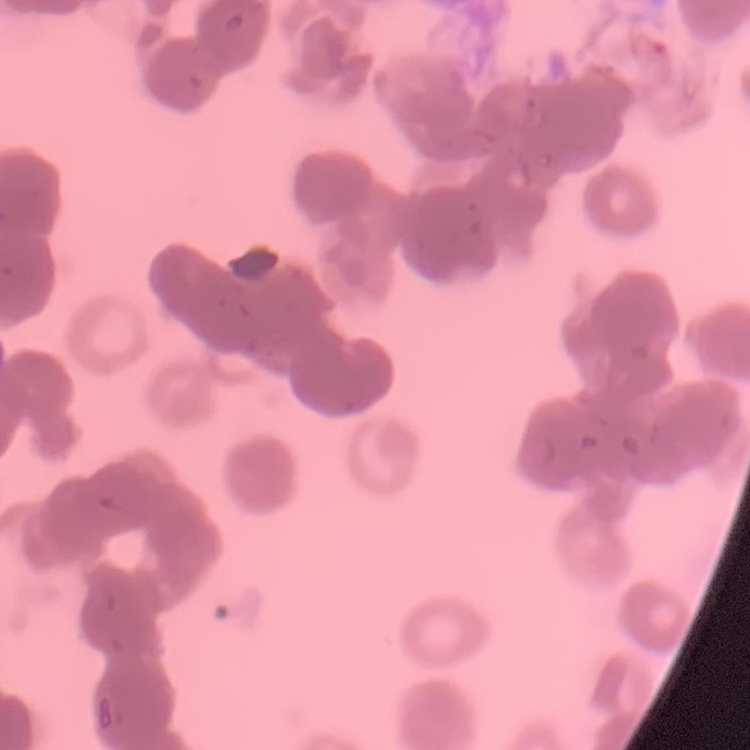
Summary:
  - Red blood cell morphology: rouleaux formation
  - Preparation: thin blood film
  - Image type: one tile cut from a larger photomicrograph
  - Stain: Field's or Giemsa